Classify this cell by malaria status.
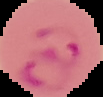
It is parasitized.

From a thin blood film. The area outside the segmented cell region is set to black. Image is 103×97 pixels.